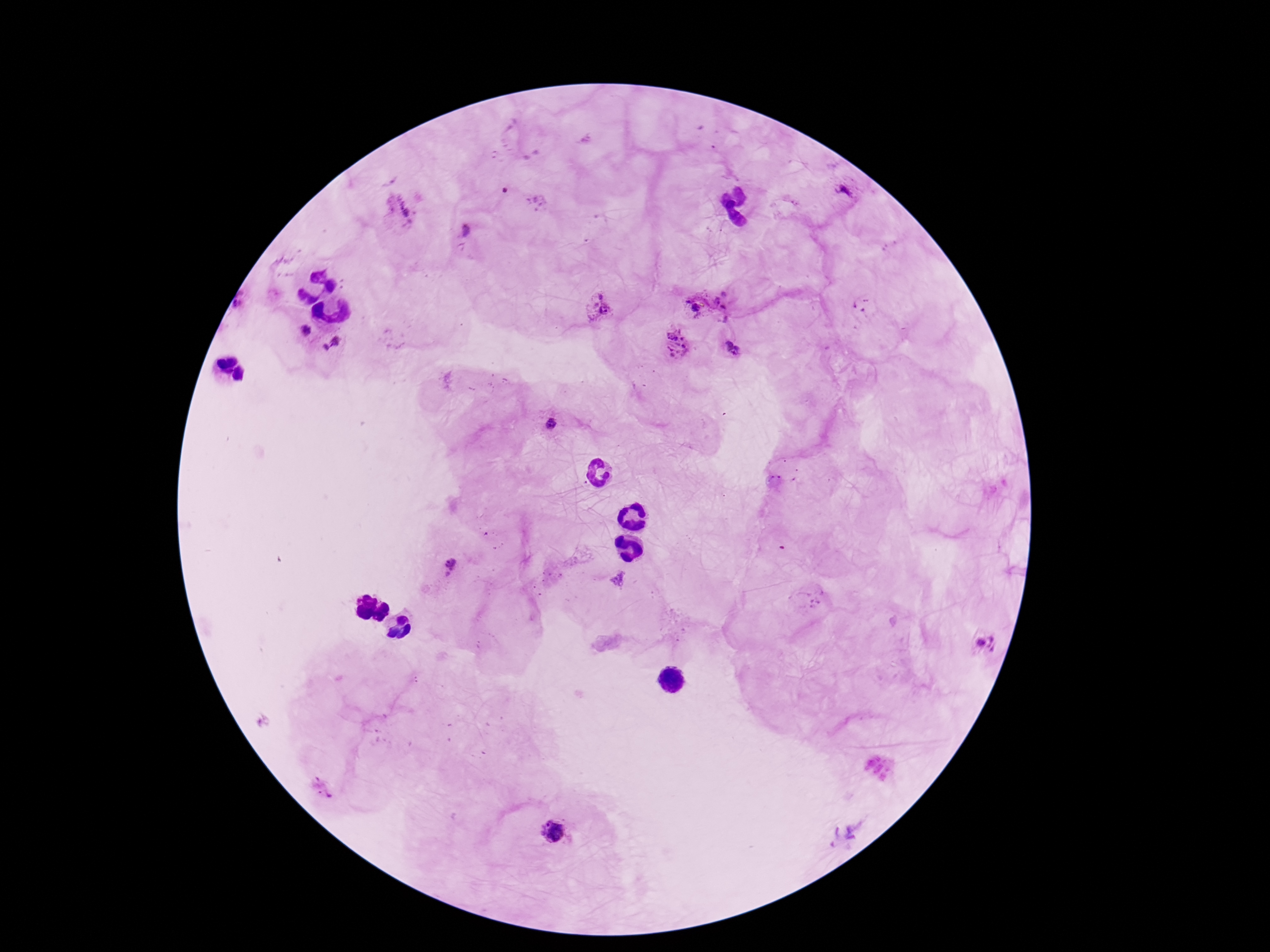
magnification = 100x
field of view = one from this slide
Plasmodium parasite locations = approximate object centers, in pixels from the top-left corner: (x=845, y=193), (x=401, y=212), (x=466, y=230), (x=729, y=305), (x=863, y=306), (x=596, y=308), (x=695, y=308), (x=304, y=331), (x=333, y=344), (x=676, y=347), (x=731, y=349), (x=552, y=424), (x=451, y=564), (x=984, y=643), (x=553, y=831), (x=844, y=833)
preparation = thick blood smear
capture = smartphone camera through the microscope eyepiece
patient malaria status = infected
image size = 1270×952 pixels
stain = Giemsa